Assess the morphology of the erythrocytes.
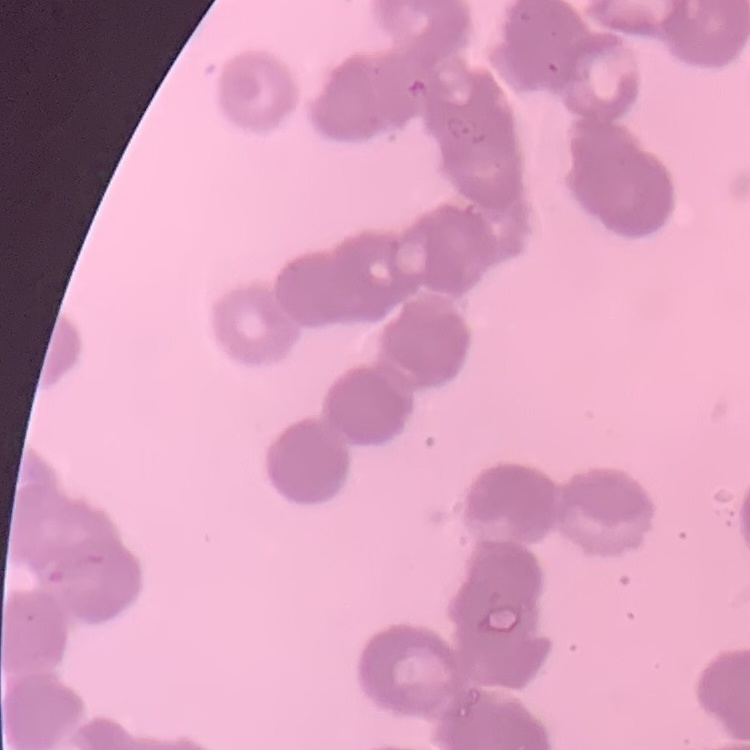
They show rouleaux formation.

Summary:
  - Stain: Field's or Giemsa
  - Image type: one tile cut from a larger photomicrograph
  - Preparation: thin blood smear